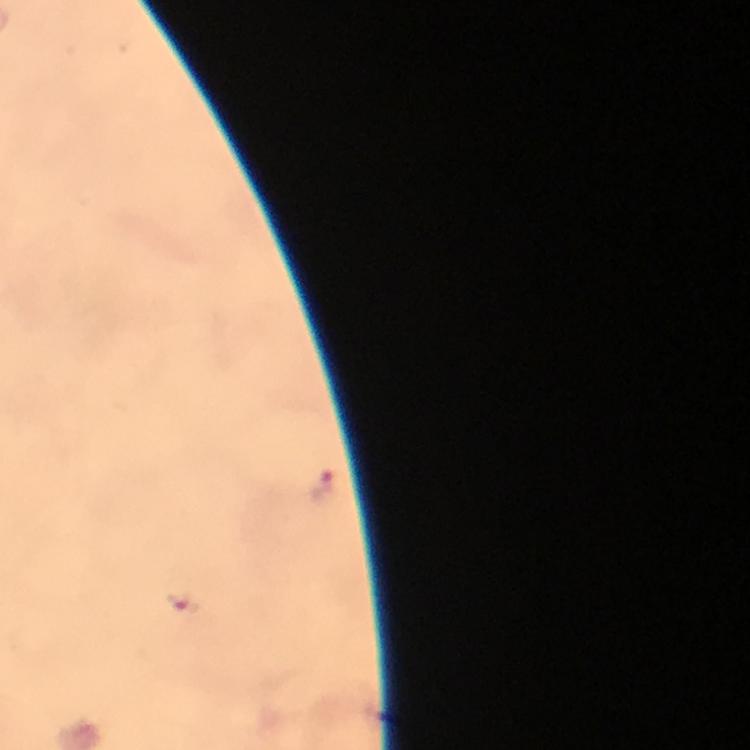
Approximate centers as {x, y} in pixels.
Summary:
  - Malaria parasite locations: {320, 484}, {182, 605}
  - Capture: smartphone photograph through a microscope
  - Preparation: thick blood smear
  - Image size: 750×750 pixels
  - Cropped from: one field of view
  - Magnification: 100x
  - Stain: Giemsa
  - Immersion oil: applied
  - Context: from a diagnostic examination for malaria